Identify the parasite.
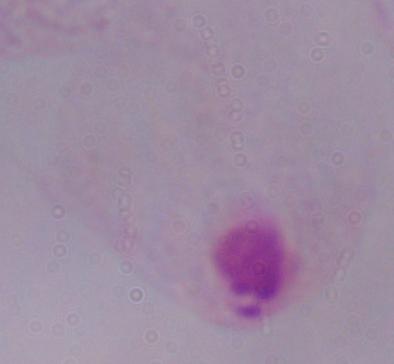
A trichomonad.

Photomicrograph. 1000x magnification.